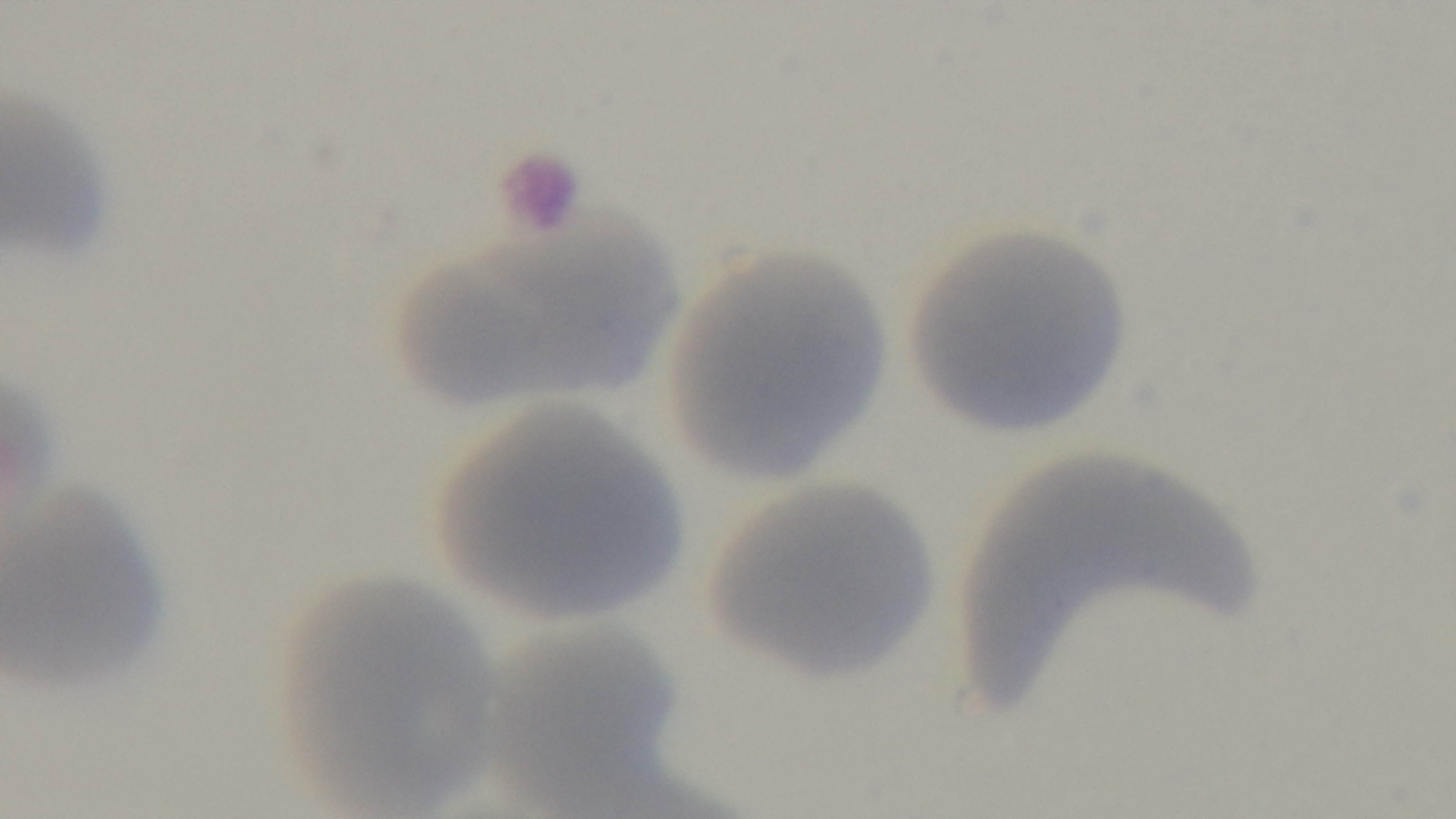 Captured with a mounted 4K digital camera. Light microscopy. Giemsa-stained. Malaria status: uninfected. One field from the slide. Preparation: thin. Oil-immersion objective, 100x.